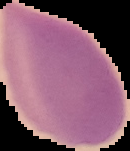
Summary:
  - Preparation: thin blood film
  - Image size: 130×151 pixels
  - Image type: segmented cell region with the area outside set to black
  - Malaria status: uninfected